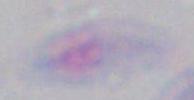
{
  "magnification": "1000x",
  "identification": "Toxoplasma gondii",
  "modality": "micrograph"
}